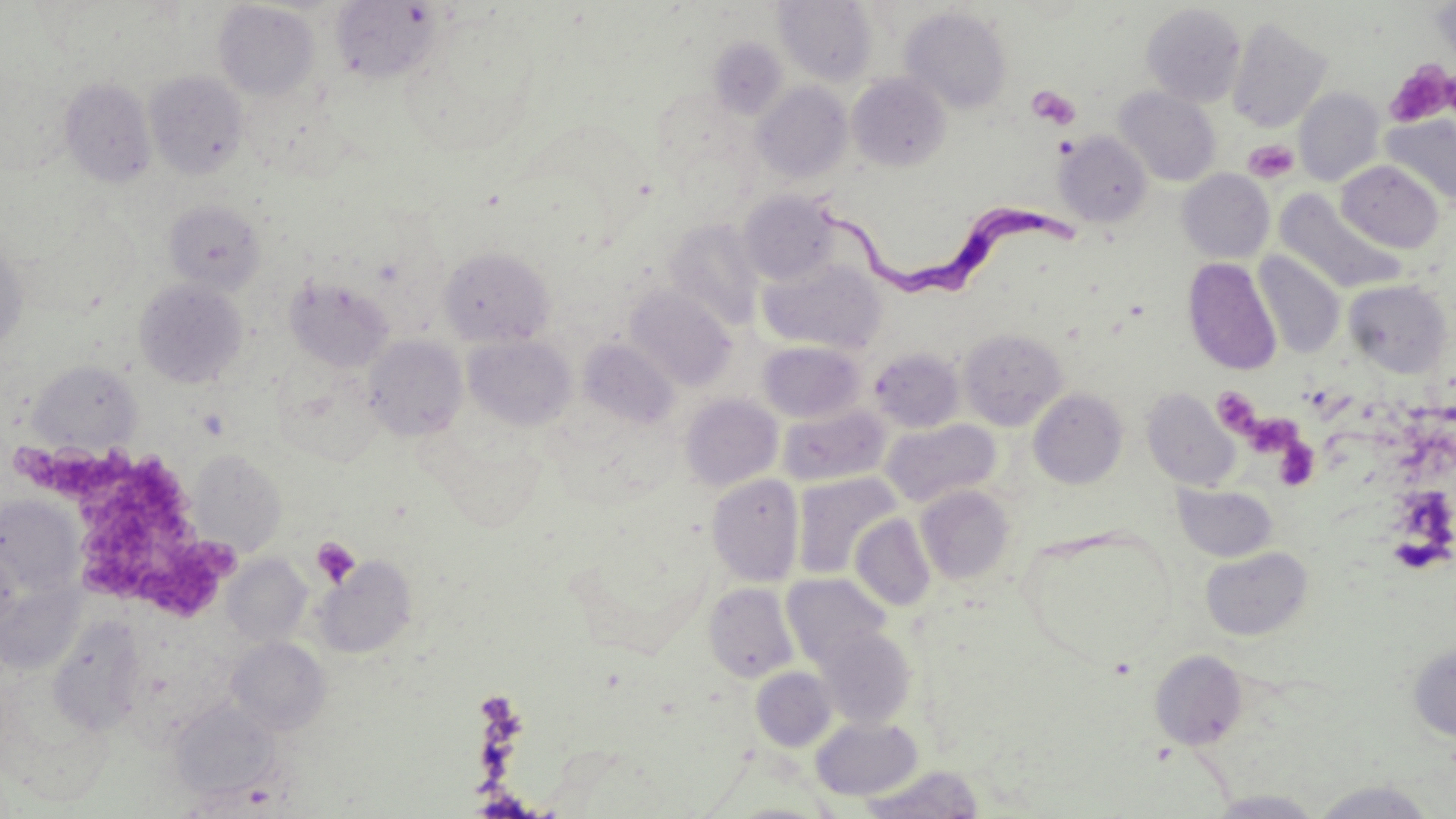

Approximate bounding boxes as named x1/y1/x2/y2 corners in pixels. Platelet locations: (x1=1384, y1=61, x2=1455, y2=128), (x1=1027, y1=86, x2=1081, y2=130), (x1=1054, y1=137, x2=1079, y2=160), (x1=1243, y1=139, x2=1301, y2=184), (x1=1211, y1=387, x2=1260, y2=435), (x1=1273, y1=439, x2=1319, y2=491), (x1=16, y1=444, x2=236, y2=616), (x1=311, y1=537, x2=360, y2=588). Uninfected red blood cell locations: (x1=774, y1=0, x2=878, y2=86), (x1=330, y1=1, x2=444, y2=84), (x1=213, y1=2, x2=321, y2=101), (x1=1141, y1=3, x2=1247, y2=107), (x1=1432, y1=3, x2=1456, y2=67), (x1=899, y1=6, x2=1013, y2=114), (x1=401, y1=15, x2=540, y2=154), (x1=1226, y1=17, x2=1333, y2=133), (x1=708, y1=37, x2=788, y2=119), (x1=145, y1=71, x2=248, y2=179), (x1=847, y1=73, x2=950, y2=171), (x1=59, y1=77, x2=157, y2=187), (x1=752, y1=82, x2=853, y2=184), (x1=1114, y1=87, x2=1221, y2=187), (x1=1294, y1=87, x2=1385, y2=186), (x1=1380, y1=114, x2=1456, y2=209), (x1=1055, y1=131, x2=1153, y2=228), (x1=1336, y1=161, x2=1444, y2=253), (x1=1177, y1=169, x2=1274, y2=263), (x1=739, y1=190, x2=840, y2=285), (x1=1274, y1=191, x2=1407, y2=294), (x1=164, y1=200, x2=266, y2=294), (x1=664, y1=218, x2=765, y2=331), (x1=0, y1=242, x2=28, y2=355), (x1=437, y1=246, x2=555, y2=347), (x1=1253, y1=251, x2=1345, y2=358), (x1=757, y1=256, x2=886, y2=354), (x1=1184, y1=258, x2=1281, y2=375), (x1=287, y1=277, x2=395, y2=371), (x1=1343, y1=278, x2=1453, y2=378), (x1=135, y1=279, x2=248, y2=388), (x1=625, y1=285, x2=736, y2=391), (x1=958, y1=327, x2=1068, y2=431), (x1=463, y1=334, x2=576, y2=430), (x1=364, y1=335, x2=467, y2=440), (x1=579, y1=338, x2=678, y2=430), (x1=757, y1=340, x2=866, y2=423), (x1=868, y1=347, x2=964, y2=433), (x1=29, y1=361, x2=142, y2=454), (x1=1028, y1=388, x2=1128, y2=489), (x1=1142, y1=388, x2=1240, y2=491), (x1=680, y1=394, x2=782, y2=491), (x1=777, y1=403, x2=890, y2=487), (x1=881, y1=419, x2=1000, y2=507), (x1=188, y1=449, x2=286, y2=557), (x1=707, y1=474, x2=804, y2=586), (x1=792, y1=474, x2=899, y2=581), (x1=1173, y1=483, x2=1278, y2=561), (x1=915, y1=485, x2=1015, y2=585), (x1=0, y1=495, x2=84, y2=599), (x1=850, y1=513, x2=936, y2=612), (x1=1018, y1=530, x2=1176, y2=670), (x1=1200, y1=545, x2=1313, y2=642), (x1=223, y1=554, x2=312, y2=647), (x1=315, y1=557, x2=416, y2=657), (x1=781, y1=573, x2=891, y2=668), (x1=703, y1=582, x2=799, y2=683), (x1=48, y1=615, x2=147, y2=736), (x1=816, y1=627, x2=916, y2=727), (x1=227, y1=637, x2=330, y2=735), (x1=1407, y1=642, x2=1456, y2=742), (x1=1148, y1=650, x2=1247, y2=749), (x1=751, y1=667, x2=837, y2=751), (x1=168, y1=699, x2=282, y2=801), (x1=811, y1=716, x2=923, y2=800), (x1=858, y1=765, x2=986, y2=818), (x1=1311, y1=780, x2=1440, y2=817), (x1=1206, y1=789, x2=1327, y2=817). Trypanosoma brucei locations: (x1=819, y1=192, x2=1083, y2=314). Slide-level diagnosis: Trypanosoma brucei. 1000x magnification. Image is 1456×819 pixels. Thin blood film. One field of a larger specimen. Optical microscopy. May-Grünwald-Giemsa-stained preparation.